Outline each Plasmodium ovale-infected red blood cell.
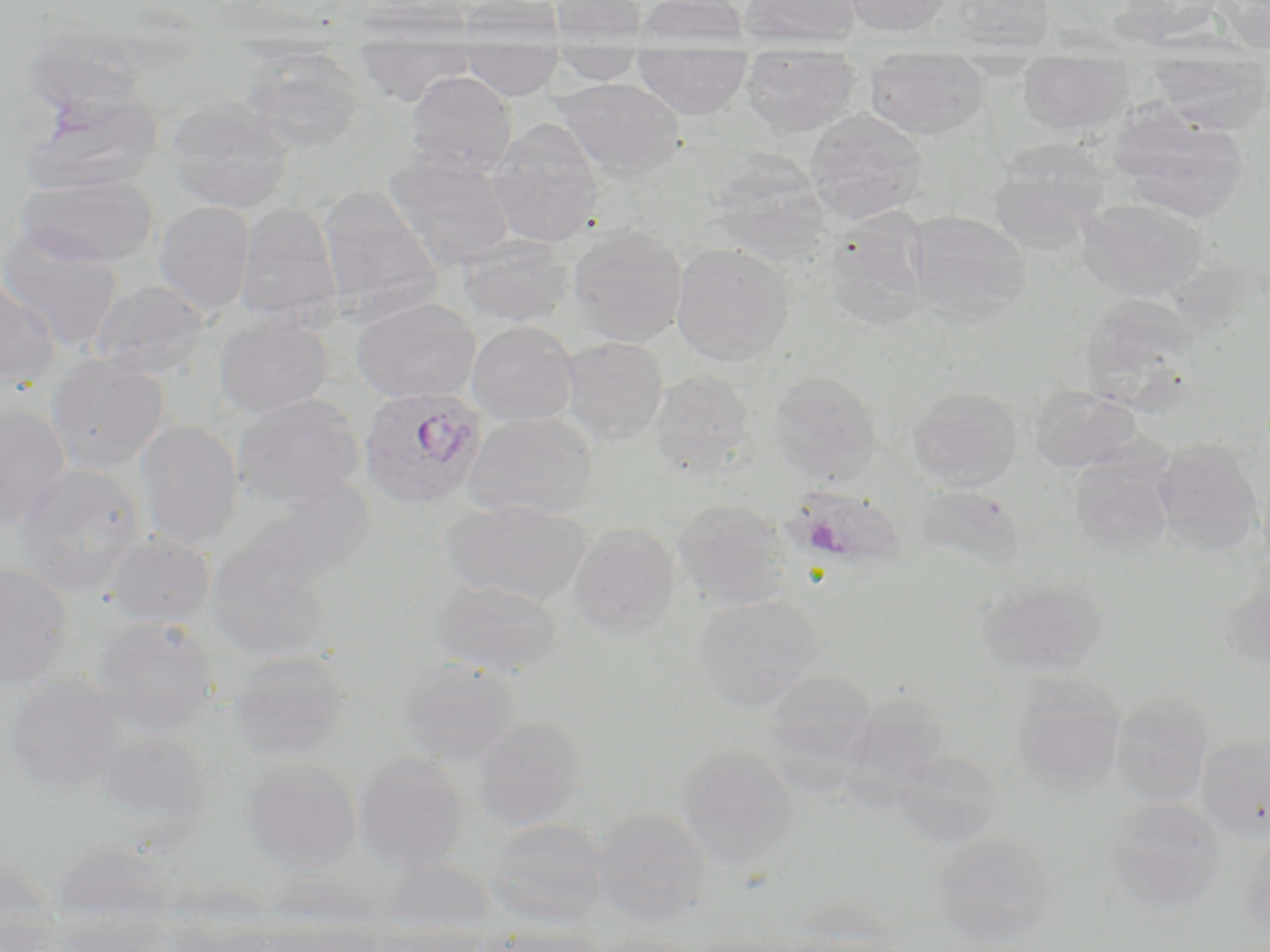

Approximate bounding boxes as (x1, y1, x2, y2) in pixels.
Plasmodium ovale-infected red blood cells: (358, 385, 489, 509).

slide-level diagnosis = Plasmodium ovale
stain = May-Grünwald-Giemsa
preparation = thin blood film
field of view = single
image size = 1270×952 pixels
modality = light microscopy
magnification = 1000x
uninfected red blood cell locations = approximate bounding boxes as (x1, y1, x2, y2) in pixels: (452, 0, 565, 46), (550, 0, 648, 46), (635, 0, 749, 48), (738, 0, 863, 47), (842, 0, 951, 36), (951, 0, 1054, 53), (1113, 0, 1225, 46), (1212, 0, 1270, 52), (21, 23, 157, 124), (242, 46, 366, 152), (354, 46, 475, 105), (462, 48, 563, 100), (549, 49, 646, 85), (634, 50, 751, 119), (740, 54, 862, 137), (865, 57, 988, 139), (1017, 59, 1132, 136), (1148, 59, 1270, 131), (405, 71, 517, 179), (553, 77, 686, 181), (21, 86, 165, 196), (167, 95, 292, 213), (1110, 104, 1249, 222), (805, 109, 927, 224), (488, 119, 604, 247), (989, 140, 1109, 253), (384, 150, 515, 269), (709, 151, 831, 263), (15, 174, 160, 267), (318, 186, 444, 329), (1078, 199, 1207, 301), (153, 201, 256, 316), (234, 202, 342, 330), (822, 209, 930, 332), (908, 211, 1032, 327), (567, 223, 688, 347), (0, 230, 124, 352), (457, 234, 574, 328), (670, 244, 794, 365), (0, 280, 61, 391), (90, 281, 210, 380), (1078, 294, 1201, 402), (351, 297, 481, 403), (215, 316, 332, 418), (466, 320, 579, 426), (561, 336, 669, 443), (45, 354, 169, 474), (650, 370, 757, 475), (769, 371, 882, 483), (1029, 384, 1140, 473), (907, 385, 1024, 490), (232, 394, 364, 508), (0, 403, 71, 530), (461, 411, 597, 521), (135, 420, 244, 549), (1154, 438, 1264, 554), (1068, 447, 1178, 556), (12, 462, 146, 592), (246, 476, 375, 585), (914, 484, 1026, 573), (791, 485, 907, 568), (441, 499, 593, 606), (673, 499, 791, 610), (569, 524, 680, 639), (103, 532, 215, 627), (205, 541, 330, 660), (1220, 555, 1270, 670), (0, 561, 73, 688), (975, 577, 1108, 678), (431, 578, 564, 678), (693, 594, 825, 711), (92, 616, 218, 736), (226, 649, 353, 759), (398, 658, 522, 765), (763, 669, 878, 780), (3, 673, 125, 796), (1012, 677, 1126, 797), (842, 690, 951, 799), (1110, 691, 1214, 807), (471, 715, 589, 828), (94, 729, 213, 833), (1196, 733, 1270, 842), (677, 743, 800, 868), (891, 750, 1002, 849), (353, 753, 469, 872), (240, 758, 361, 874), (1102, 797, 1226, 915), (590, 806, 712, 924), (486, 817, 612, 928), (1237, 830, 1270, 944), (929, 831, 1057, 945), (0, 859, 62, 951), (49, 918, 178, 952), (166, 919, 285, 952), (486, 926, 608, 952), (584, 935, 703, 952)